Locate every blood parasite and identify its species.
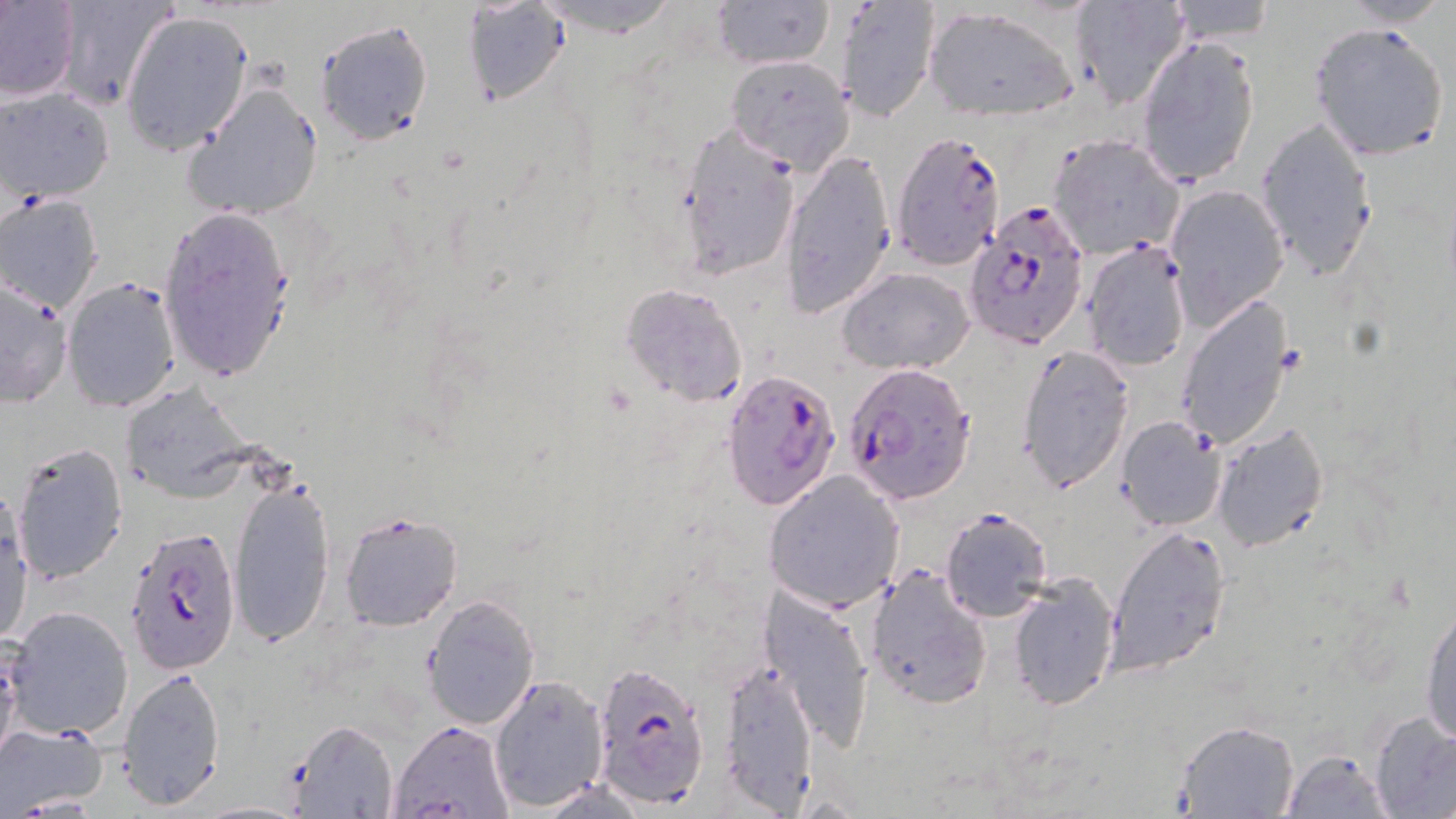
Approximate bounding boxes as [x1, y1, x2, y2] in pixels.
Plasmodium falciparum-infected red blood cells: [890, 128, 1007, 271], [963, 201, 1091, 351], [843, 363, 976, 507], [721, 367, 842, 512], [125, 524, 244, 677], [590, 660, 711, 809].
No Plasmodium ovale, Plasmodium malariae, Plasmodium vivax, Babesia divergens, or Trypanosoma brucei observed.

Summary:
  - Uninfected red blood cell locations: [0, 0, 80, 102], [55, 0, 176, 109], [460, 0, 575, 107], [712, 0, 832, 70], [1161, 0, 1279, 47], [535, 1, 681, 37], [1068, 1, 1192, 109], [1336, 1, 1455, 27], [839, 2, 938, 122], [924, 7, 1080, 121], [118, 11, 253, 156], [315, 18, 433, 145], [1308, 22, 1451, 162], [1135, 35, 1261, 187], [724, 54, 855, 172], [184, 80, 324, 222], [2, 87, 115, 203], [1255, 117, 1379, 280], [675, 120, 800, 278], [1046, 134, 1186, 261], [779, 150, 897, 322], [1163, 184, 1288, 326], [0, 194, 104, 311], [156, 207, 297, 383], [1084, 241, 1190, 370], [836, 266, 975, 374], [61, 277, 180, 413], [0, 279, 72, 409], [617, 282, 747, 406], [1174, 297, 1297, 451], [1017, 344, 1135, 495], [119, 380, 257, 501], [1115, 415, 1225, 532], [1212, 424, 1329, 552], [11, 440, 127, 585], [764, 470, 906, 613], [229, 475, 335, 650], [0, 493, 33, 647], [940, 507, 1053, 622], [338, 509, 464, 631], [1108, 524, 1230, 678], [866, 566, 992, 708], [1008, 573, 1121, 711], [761, 586, 877, 751], [421, 594, 541, 729], [1419, 597, 1456, 748], [4, 606, 132, 739], [0, 644, 20, 771], [721, 656, 818, 810], [118, 666, 226, 811], [487, 675, 610, 812], [1369, 711, 1456, 818], [289, 719, 398, 819], [389, 720, 513, 818], [1174, 720, 1300, 819], [0, 725, 109, 814], [1279, 750, 1394, 818], [192, 801, 310, 817]
  - Slide-level diagnosis: Plasmodium falciparum
  - Image size: 1456×819 pixels
  - Field of view: single
  - Stain: May-Grünwald-Giemsa
  - Magnification: 1000x
  - Modality: optical microscopy
  - Preparation: thin blood smear